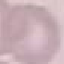

malaria_status: uninfected
capture: smartphone camera at the microscope eyepiece
image_type: automatically extracted cell patch, resized to 64 × 64 pixels
preparation: thin blood smear
stain: Giemsa